Give the position of every malaria parasite.
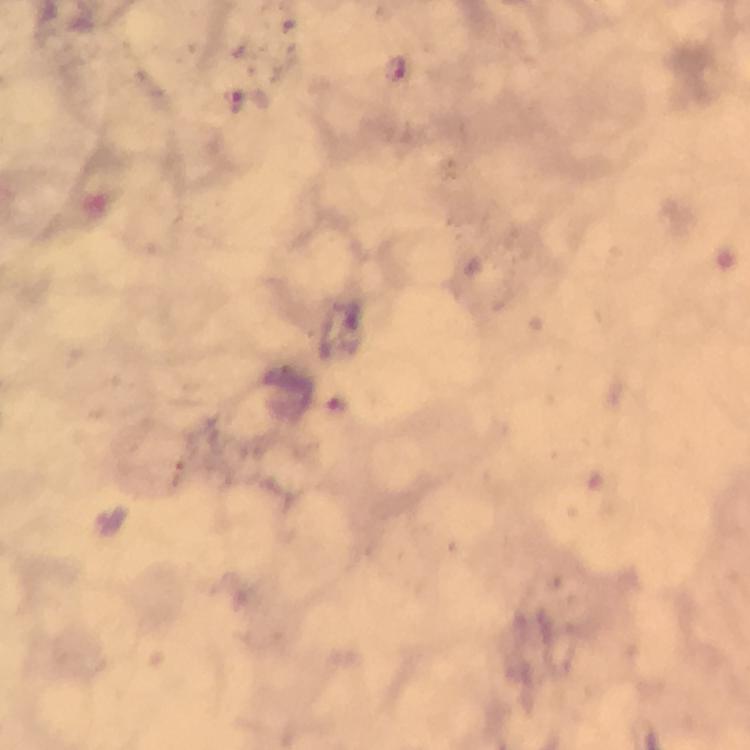
Approximate centers as [x, y] in pixels.
Malaria parasites: [396, 69], [252, 103].

image_size: 750×750 pixels
magnification: 100x
context: from a malaria diagnostic workup
capture: smartphone photograph through a microscope
immersion_oil: applied
preparation: thick blood film
stain: Giemsa
cropped_from: one field of view